Classify this cell by malaria status.
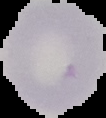

Uninfected.

image_size: 106×118 pixels
preparation: thin blood film
image_type: cell region segmented out of the field of view; surrounding area masked to black